Classify this cell by malaria status.
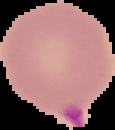
It is parasitized.

Summary:
  - Image type: segmented cell region with the area outside set to black
  - Preparation: thin blood smear
  - Image size: 115×130 pixels